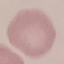

Summary:
  - Result: no malaria parasites seen
  - Preparation: thin smear
  - Stain: Giemsa
  - Image type: automatically extracted cell patch, resized to 64 × 64 pixels
  - Capture: smartphone camera at the microscope eyepiece